Describe the morphology of the red blood cells.
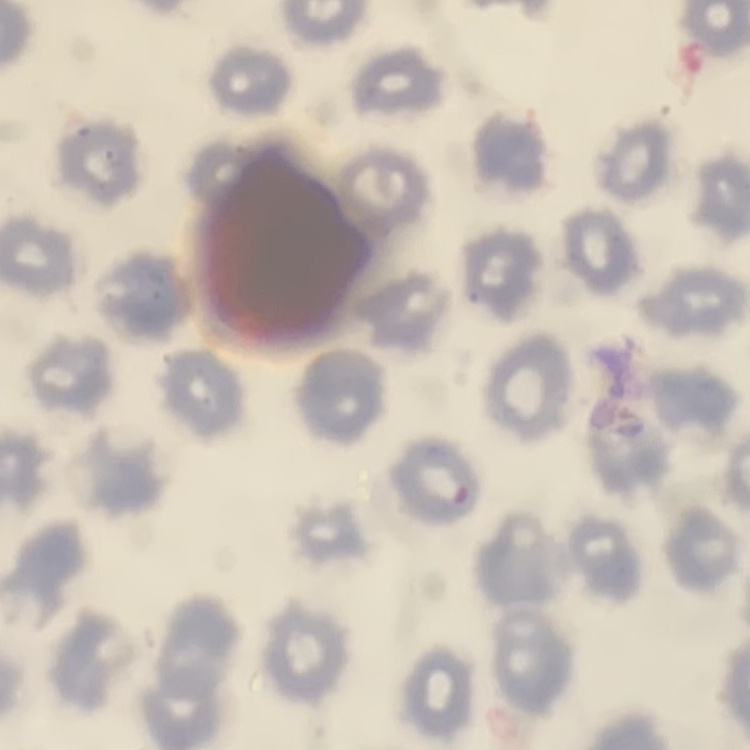

They show no rouleaux formation.

Summary:
  - Stain: Field's or Giemsa
  - Preparation: thin peripheral smear
  - Image type: one tile cut from a larger photomicrograph